Report the malaria status of this cell.
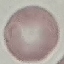
It is uninfected.

Summary:
  - Capture: smartphone through the microscope eyepiece
  - Image type: automatically extracted cell patch, resized to 64 × 64 pixels
  - Preparation: thin smear
  - Stain: Giemsa